Comment on the morphology of the erythrocytes.
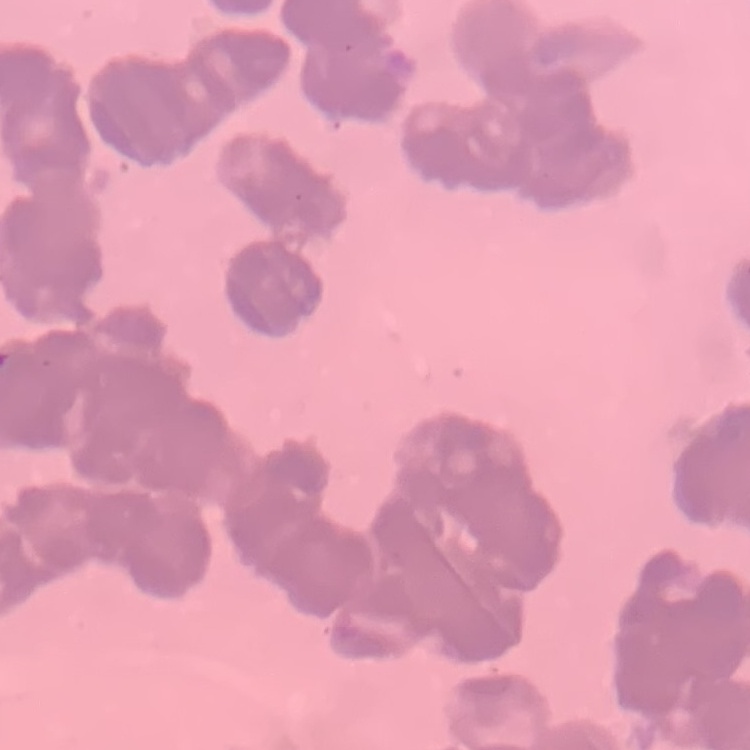
Rouleaux formation.

Summary:
  - Preparation: thin blood smear
  - Stain: Field's or Giemsa
  - Image type: one tile cut from a larger photomicrograph